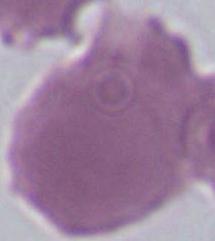
magnification: 1000x
modality: photomicrograph
identification: erythrocyte